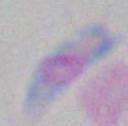
identification: Toxoplasma gondii
magnification: 1000x
modality: micrograph